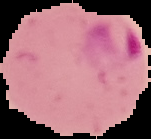
image size = 151×139 pixels
image type = segmented cell region on a black background
preparation = thin blood smear
result = malaria parasites detected